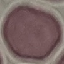

Summary:
  - Malaria status: uninfected
  - Preparation: thin blood smear
  - Image type: cell patch, automatically extracted from a larger field of view and resized to 64 × 64 pixels
  - Stain: Giemsa
  - Capture: smartphone through the microscope eyepiece